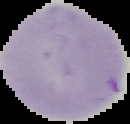

Summary:
  - Image size: 130×124 pixels
  - Result: negative for Plasmodium parasites
  - Preparation: thin blood smear
  - Image type: cell region segmented out of the field of view; surrounding area masked to black